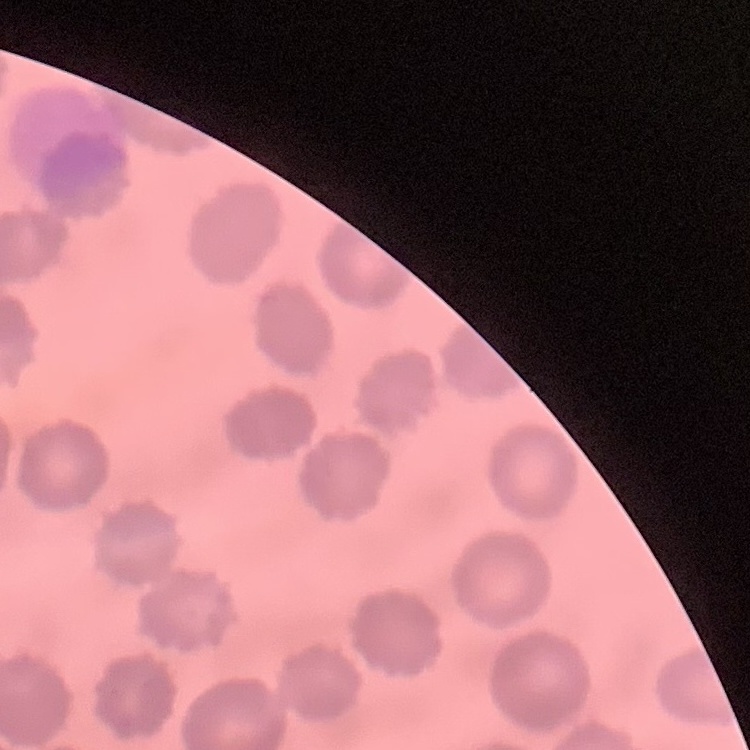
red blood cell morphology = no rouleaux formation
stain = Field's or Giemsa
image type = one tile cut from a larger photomicrograph
preparation = thin peripheral smear